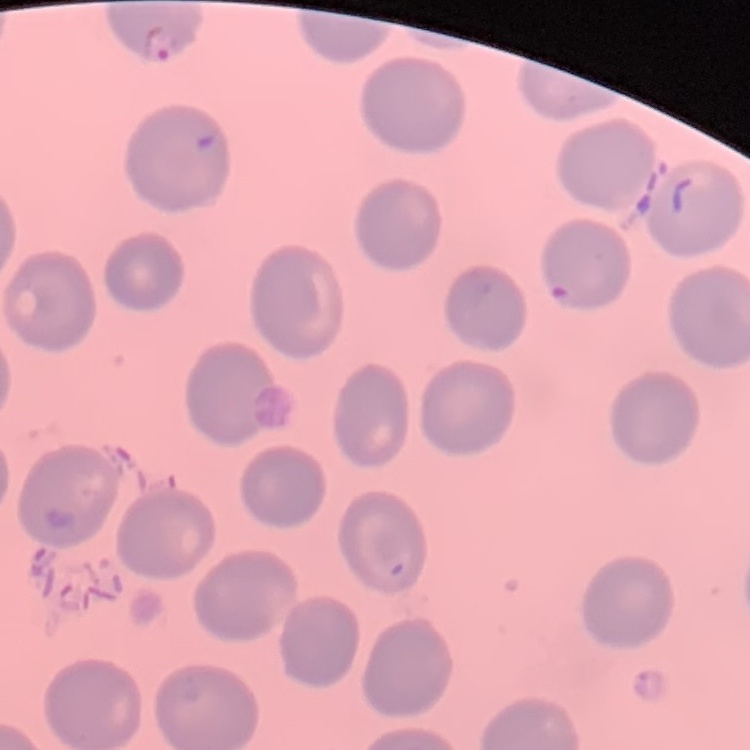
red blood cell morphology = no rouleaux formation
image type = square crop of a larger photomicrograph
stain = Field's or Giemsa
preparation = thin blood smear